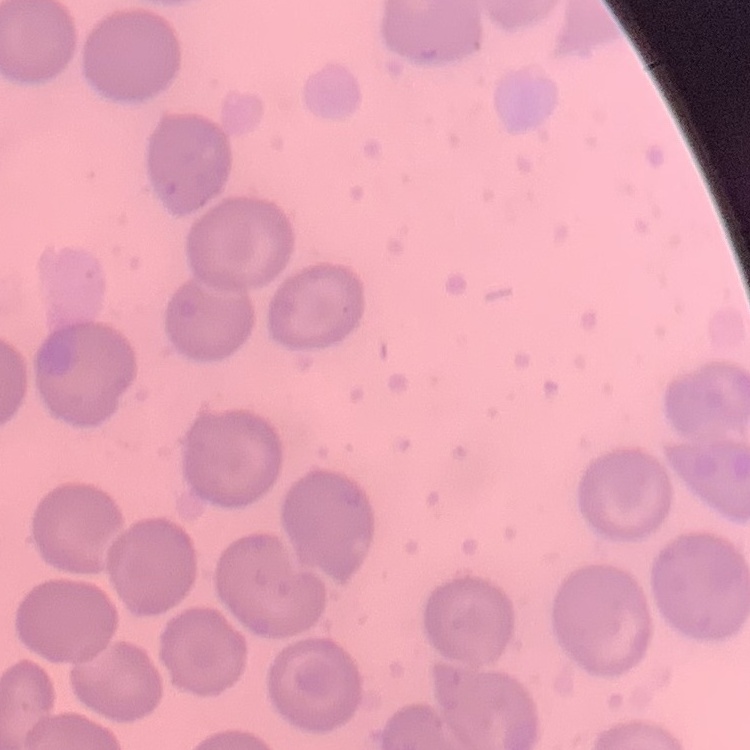

Summary:
  - Erythrocyte morphology: no rouleaux formation
  - Preparation: thin blood smear
  - Stain: Field's or Giemsa
  - Image type: square crop of a larger photomicrograph